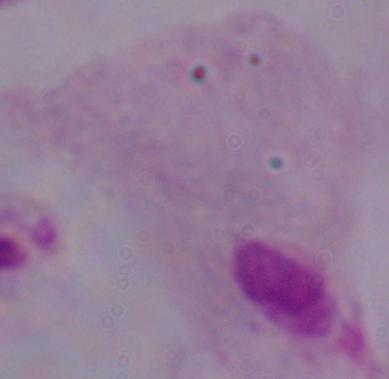
1000x magnification. A trichomonad is seen. Micrograph.